Classify this cell by malaria status.
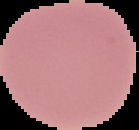
Uninfected.

Summary:
  - Image size: 139×130 pixels
  - Preparation: thin blood film
  - Image type: segmented cell region with the area outside set to black